Assess this cell for malaria.
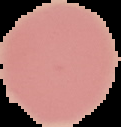

It is uninfected.

Summary:
  - Image type: segmented cell region on a black background
  - Preparation: thin blood film
  - Image size: 121×127 pixels